Assess this cell for malaria.
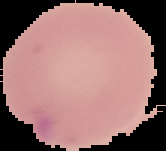

Parasitized.

{
  "image_type": "cell region segmented out of the field of view; surrounding area masked to black",
  "image_size": "166×151 pixels",
  "preparation": "thin blood film"
}